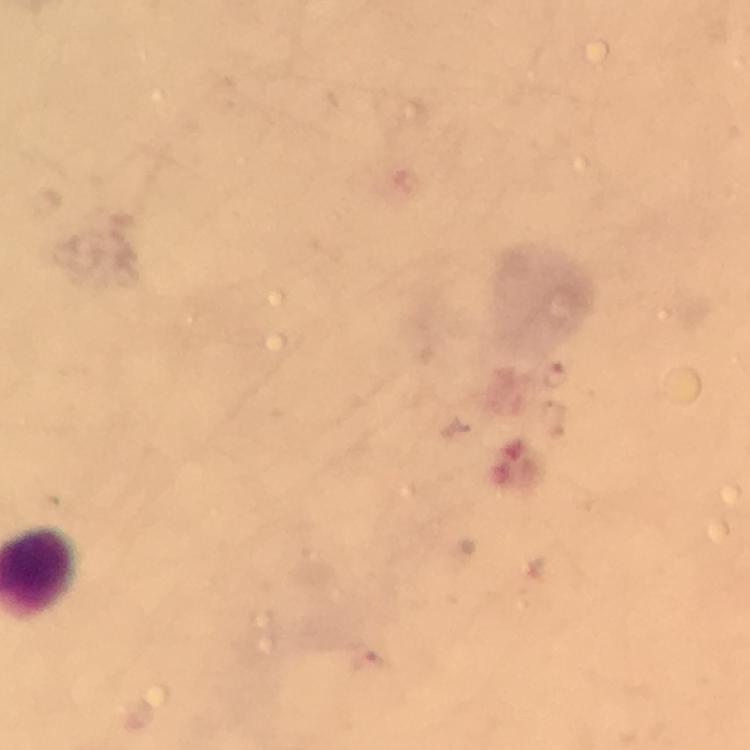

Approximate centers as [x, y] in pixels.
Summary:
  - Plasmodium parasite locations: [557, 375]
  - Context: from a diagnostic examination for malaria
  - Cropped from: a single field of view
  - Magnification: 100x
  - Capture: smartphone mounted on the microscope
  - Immersion oil: applied
  - Stain: Giemsa
  - Preparation: thick smear
  - Image size: 750×750 pixels